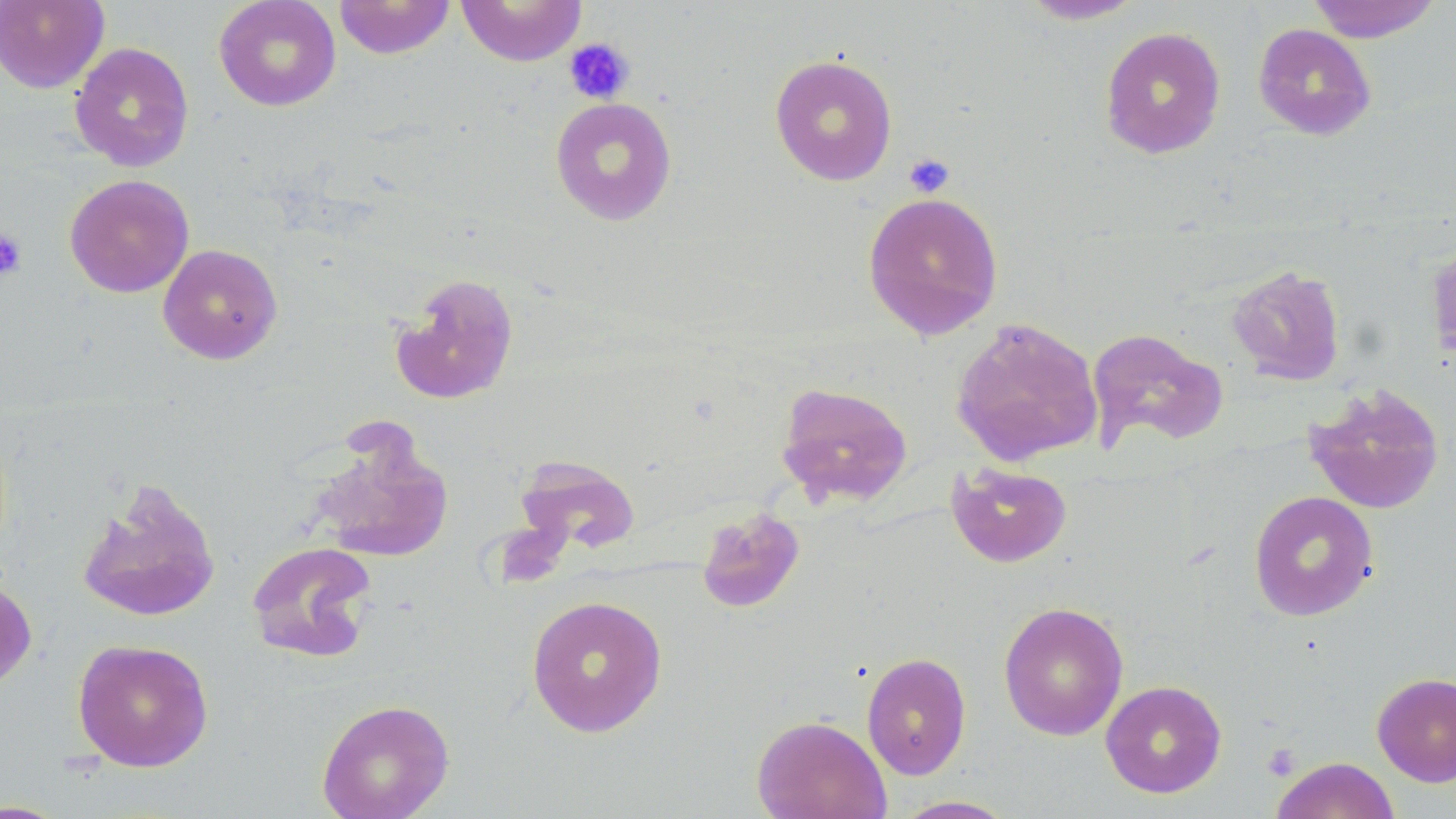
Summary:
  - Coordinate format: approximate bounding boxes as named x1/y1/x2/y2 corners in pixels
  - Platelet locations: (x1=564, y1=37, x2=635, y2=104), (x1=903, y1=152, x2=955, y2=198), (x1=0, y1=228, x2=27, y2=280), (x1=1261, y1=743, x2=1302, y2=781)
  - Uninfected red blood cell locations: (x1=0, y1=0, x2=109, y2=94), (x1=213, y1=0, x2=341, y2=112), (x1=334, y1=0, x2=455, y2=59), (x1=455, y1=0, x2=588, y2=66), (x1=1016, y1=0, x2=1148, y2=25), (x1=1306, y1=0, x2=1444, y2=43), (x1=1252, y1=22, x2=1377, y2=141), (x1=1099, y1=26, x2=1226, y2=159), (x1=69, y1=41, x2=195, y2=172), (x1=768, y1=54, x2=898, y2=186), (x1=550, y1=96, x2=677, y2=226), (x1=64, y1=174, x2=194, y2=298), (x1=862, y1=191, x2=1004, y2=340), (x1=1425, y1=236, x2=1456, y2=375), (x1=157, y1=243, x2=282, y2=365), (x1=1226, y1=264, x2=1347, y2=385), (x1=389, y1=272, x2=520, y2=405), (x1=951, y1=317, x2=1103, y2=467), (x1=1087, y1=327, x2=1229, y2=453), (x1=776, y1=381, x2=913, y2=508), (x1=1304, y1=383, x2=1445, y2=515), (x1=307, y1=425, x2=455, y2=564), (x1=509, y1=452, x2=641, y2=559), (x1=947, y1=462, x2=1072, y2=568), (x1=76, y1=477, x2=221, y2=623), (x1=1248, y1=490, x2=1379, y2=621), (x1=695, y1=506, x2=806, y2=614), (x1=246, y1=540, x2=377, y2=663), (x1=0, y1=575, x2=37, y2=691), (x1=525, y1=594, x2=668, y2=737), (x1=998, y1=600, x2=1129, y2=741), (x1=72, y1=638, x2=214, y2=771), (x1=861, y1=651, x2=972, y2=780), (x1=1371, y1=671, x2=1456, y2=786), (x1=1100, y1=679, x2=1227, y2=798), (x1=316, y1=697, x2=455, y2=819), (x1=752, y1=714, x2=891, y2=819), (x1=1270, y1=756, x2=1401, y2=819), (x1=890, y1=795, x2=1020, y2=818), (x1=0, y1=798, x2=71, y2=818)
  - Slide-level diagnosis: negative for blood parasites
  - Magnification: 1000x
  - Preparation: thin blood smear
  - Field of view: single
  - Modality: light microscopy
  - Stain: May-Grünwald-Giemsa
  - Image size: 1456×819 pixels